Identify the blood parasite species.
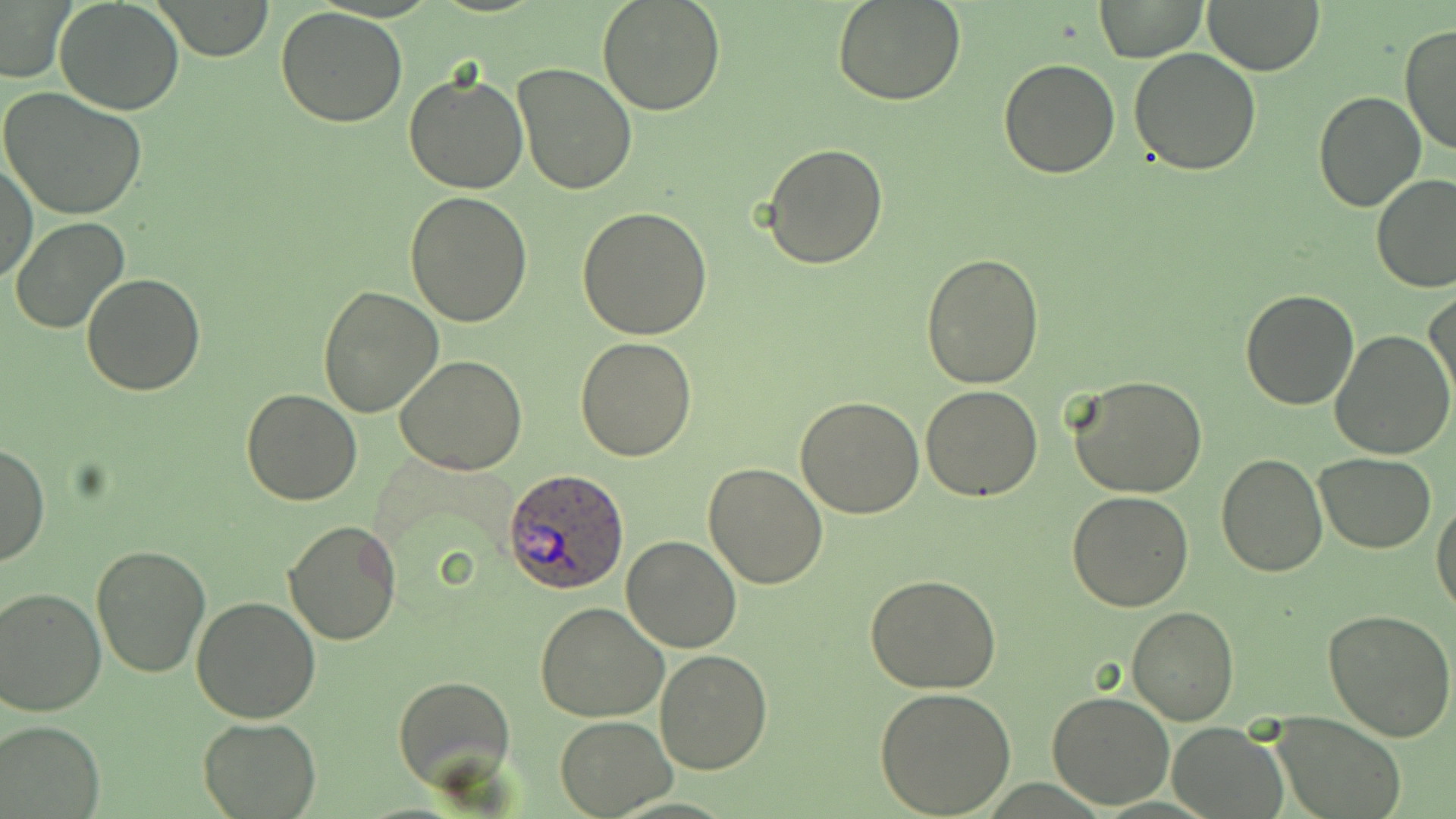

Plasmodium ovale.

Summary:
  - Coordinate format: approximate bounding boxes as (x1, y1, x2, y2) in pixels
  - Uninfected red blood cell locations: (597, 0, 727, 117), (832, 0, 967, 107), (1095, 0, 1207, 63), (55, 1, 185, 116), (153, 1, 275, 61), (1205, 2, 1323, 74), (0, 3, 72, 83), (277, 8, 409, 128), (1400, 24, 1456, 158), (1128, 48, 1261, 175), (998, 56, 1120, 178), (512, 63, 637, 194), (404, 70, 530, 193), (1, 88, 147, 221), (1313, 91, 1425, 211), (762, 141, 888, 268), (0, 160, 37, 284), (1371, 174, 1456, 293), (403, 191, 532, 327), (577, 207, 715, 339), (9, 216, 129, 335), (919, 252, 1044, 389), (79, 272, 206, 395), (318, 286, 443, 418), (1239, 288, 1360, 410), (1426, 290, 1455, 410), (1331, 331, 1455, 461), (574, 337, 698, 462), (395, 355, 527, 476), (1068, 376, 1208, 499), (918, 385, 1044, 502), (241, 389, 364, 507), (796, 395, 925, 519), (1, 443, 48, 567), (1215, 453, 1329, 577), (1315, 454, 1437, 552), (702, 461, 830, 589), (1066, 491, 1195, 611), (1432, 496, 1456, 619), (283, 520, 402, 645), (622, 536, 742, 654), (91, 543, 211, 678), (543, 565, 737, 709), (865, 574, 1000, 695), (0, 587, 105, 716), (190, 596, 322, 722), (534, 602, 669, 722), (1127, 606, 1239, 726), (1322, 608, 1456, 742), (655, 649, 774, 775), (393, 674, 518, 797), (875, 686, 1017, 817), (1047, 690, 1176, 809), (1271, 712, 1405, 819), (554, 715, 674, 817), (196, 716, 323, 818), (0, 719, 104, 817), (1169, 721, 1283, 818)
  - Plasmodium ovale-infected red blood cell locations: (502, 469, 631, 594)
  - Field of view: single
  - Modality: optical microscopy
  - Preparation: thin blood film
  - Image size: 1456×819 pixels
  - Stain: May-Grünwald-Giemsa
  - Magnification: 1000x